Report the malaria status of this cell.
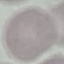

It is uninfected.

Summary:
  - Preparation: thin blood smear
  - Stain: Giemsa
  - Image type: cell patch, automatically extracted from a larger field of view and resized to 64 × 64 pixels
  - Capture: smartphone through the microscope eyepiece